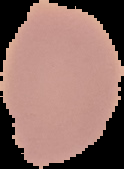

Malaria status: uninfected. Image is 124×169 pixels. Segmented cell region on a black background. From a thin blood smear.